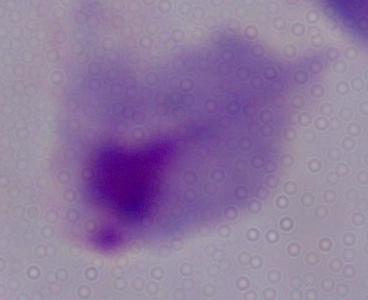

A trichomonad is shown. Photomicrograph. Captured at 1000x magnification.